Describe the morphology of the red blood cells.
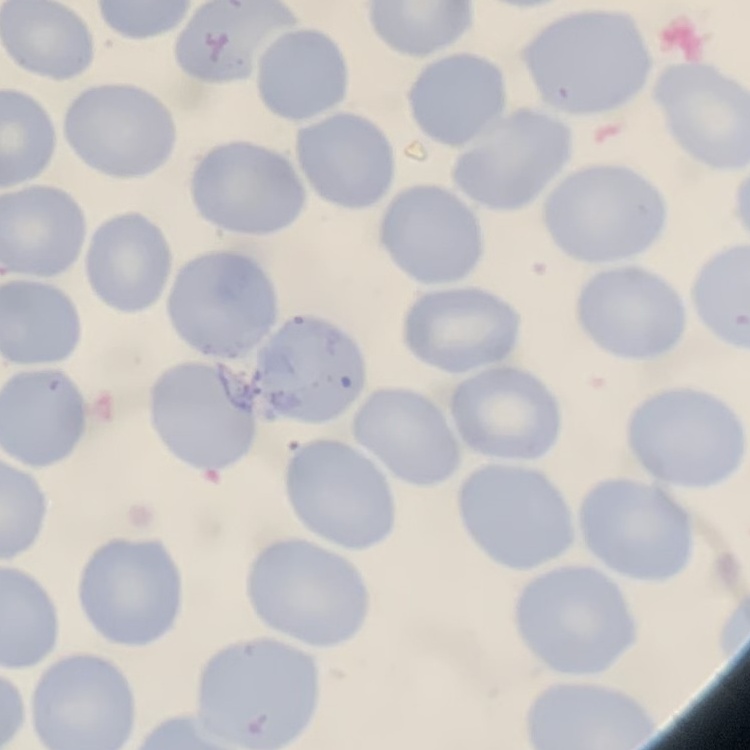

No rouleaux formation.

One tile cut from a larger photomicrograph. Stained with either Field's or Giemsa. Thin peripheral smear.